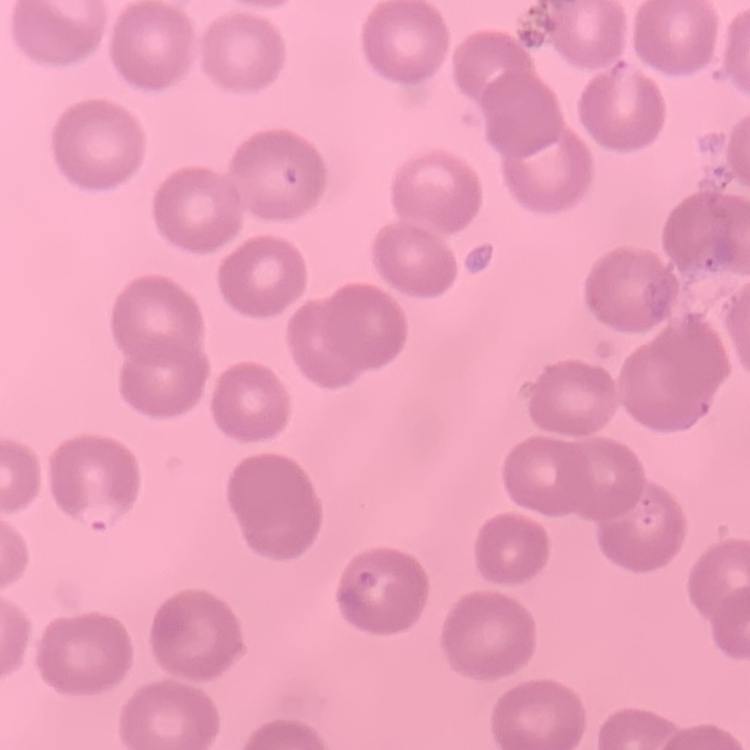

The red blood cells show no rouleaux formation. Stained with either Field's or Giemsa. Thin blood film. One tile cut from a larger photomicrograph.